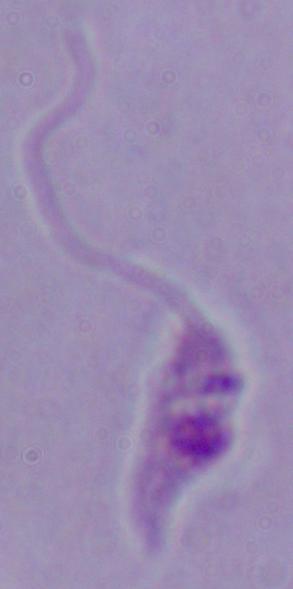
Summary:
  - Magnification: 1000x
  - Identification: Leishmania
  - Modality: micrograph